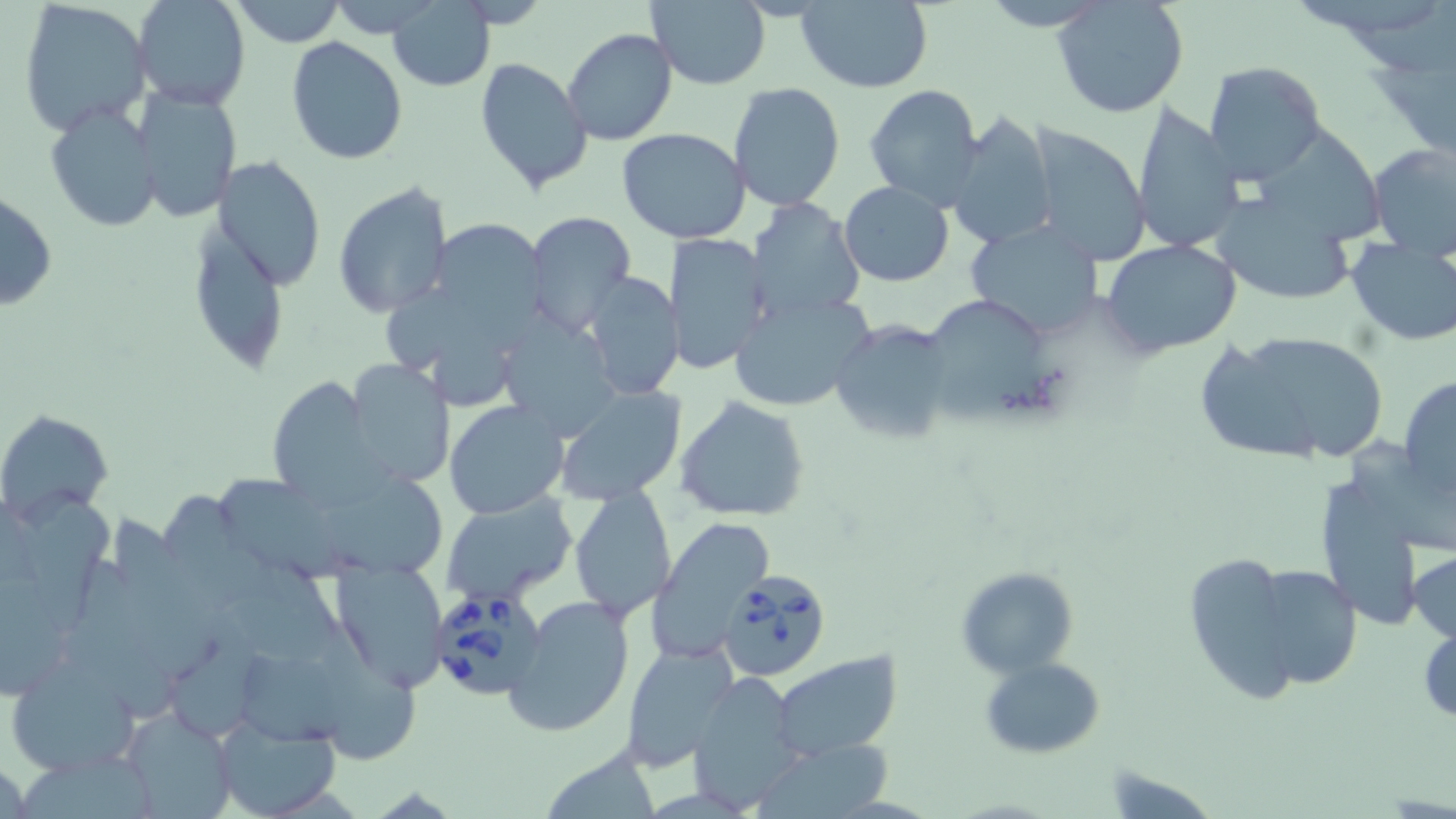
Summary:
  - Coordinate format: approximate bounding boxes as (x1,y1)-(x2,y2) corner pairs in pixels
  - Uninfected red blood cell locations: (132,0)-(250,110), (230,0)-(344,46), (645,0)-(771,89), (795,0)-(933,93), (1051,0)-(1190,119), (1335,0)-(1455,71), (16,1)-(150,134), (973,2)-(1117,30), (389,3)-(494,91), (563,28)-(677,145), (286,37)-(408,165), (1367,54)-(1456,153), (475,56)-(592,193), (1203,61)-(1327,184), (728,82)-(847,212), (863,84)-(985,210), (135,86)-(242,224), (1131,99)-(1244,257), (44,100)-(162,234), (945,109)-(1057,250), (1251,113)-(1388,246), (617,126)-(752,244), (1023,128)-(1152,266), (1366,142)-(1456,256), (212,156)-(326,292), (839,181)-(954,286), (333,183)-(455,318), (1,189)-(57,312), (1217,198)-(1362,305), (747,199)-(865,323), (196,210)-(282,370), (522,212)-(637,338), (964,217)-(1107,339), (436,218)-(556,343), (664,233)-(772,375), (1100,238)-(1244,354), (1346,240)-(1456,346), (581,271)-(684,401), (382,285)-(523,420), (506,292)-(620,435), (729,292)-(872,412), (918,292)-(1066,427), (828,319)-(958,446), (1260,334)-(1386,462), (1204,347)-(1321,452), (343,359)-(453,489), (265,375)-(387,504), (1398,375)-(1456,498), (556,384)-(686,505), (674,394)-(811,521), (444,398)-(568,520), (1,409)-(114,522), (314,465)-(442,581), (1308,468)-(1431,631), (221,470)-(349,585), (155,483)-(286,613), (14,486)-(111,634), (570,486)-(676,622), (439,492)-(577,607), (114,510)-(226,680), (648,516)-(774,661), (1408,549)-(1456,647), (1182,550)-(1312,706), (220,551)-(364,661), (74,558)-(175,728), (329,558)-(449,694), (1237,561)-(1367,695), (954,566)-(1078,676), (0,567)-(75,700), (506,596)-(635,738), (1417,617)-(1455,731), (319,618)-(421,761), (175,627)-(272,738), (620,641)-(738,769), (240,647)-(378,747), (770,651)-(905,760), (980,656)-(1105,758), (7,657)-(138,778), (687,674)-(808,812), (123,710)-(236,819), (212,714)-(342,819), (755,739)-(893,817), (539,746)-(659,817), (23,757)-(159,819)
  - Babesia divergens-infected red blood cell locations: (723,569)-(831,682), (427,588)-(550,703)
  - Slide-level diagnosis: Babesia divergens
  - Modality: optical microscopy
  - Magnification: 1000x
  - Stain: May-Grünwald-Giemsa
  - Image size: 1456×819 pixels
  - Preparation: thin blood smear
  - Field of view: single